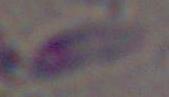

modality = photomicrograph
identification = Toxoplasma gondii
magnification = 1000x